Give the position of every leukocyte visible.
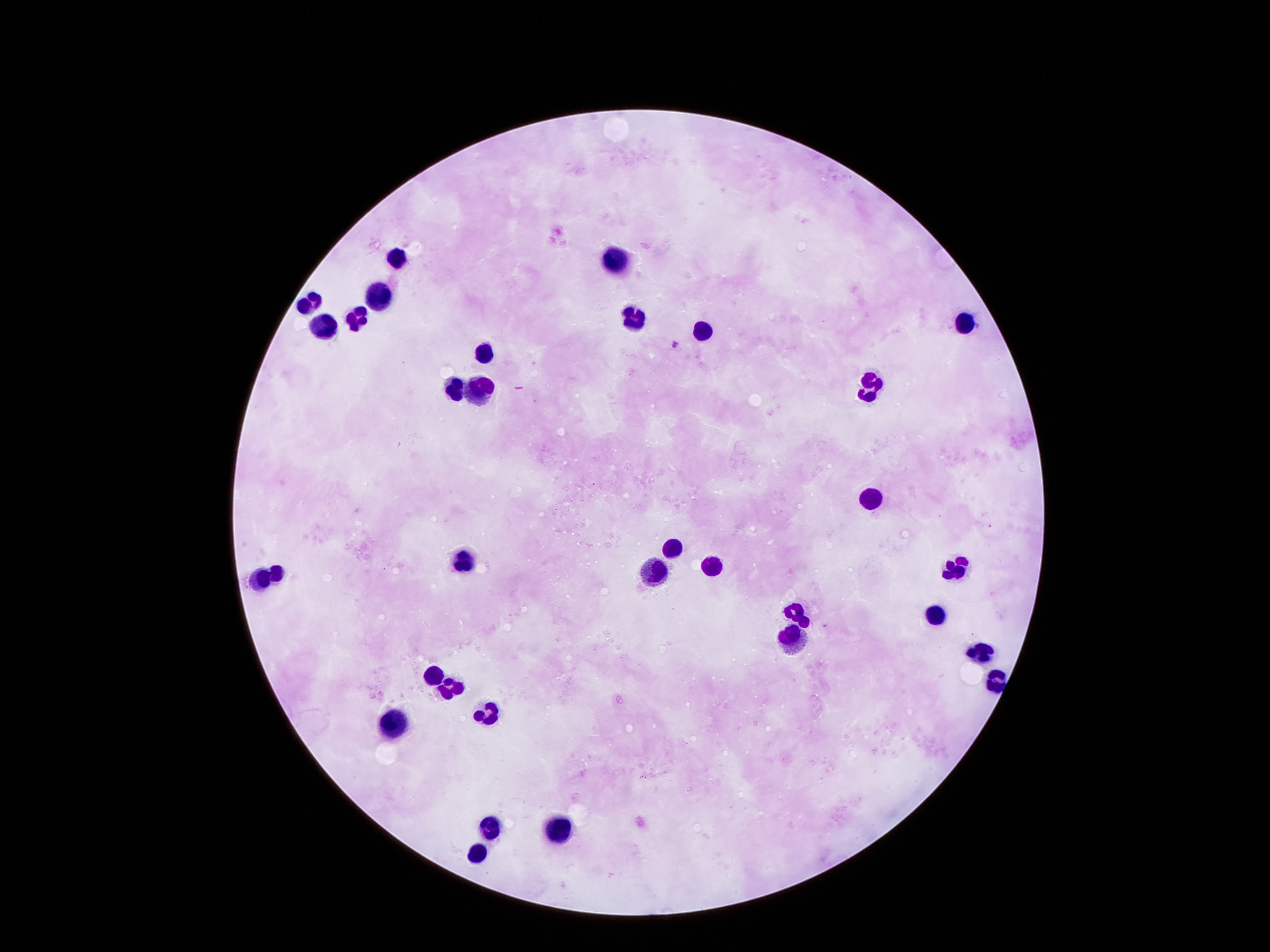

Approximate centers as {x, y} in pixels.
Leukocytes: {397, 254}, {612, 259}, {379, 294}, {312, 302}, {357, 316}, {630, 317}, {707, 324}, {963, 324}, {328, 326}, {488, 350}, {458, 382}, {474, 383}, {872, 384}, {871, 494}, {671, 550}, {657, 564}, {712, 564}, {465, 565}, {958, 568}, {276, 570}, {259, 577}, {938, 612}, {981, 654}, {431, 671}, {994, 681}, {452, 691}, {492, 707}, {390, 721}, {556, 823}, {491, 825}, {476, 855}.

Single field of view. Image is 1270×952 pixels. 100x magnification. Photographed through the microscope eyepiece with a smartphone camera. Patient malaria status: not infected. Thick blood smear. Giemsa-stained preparation.